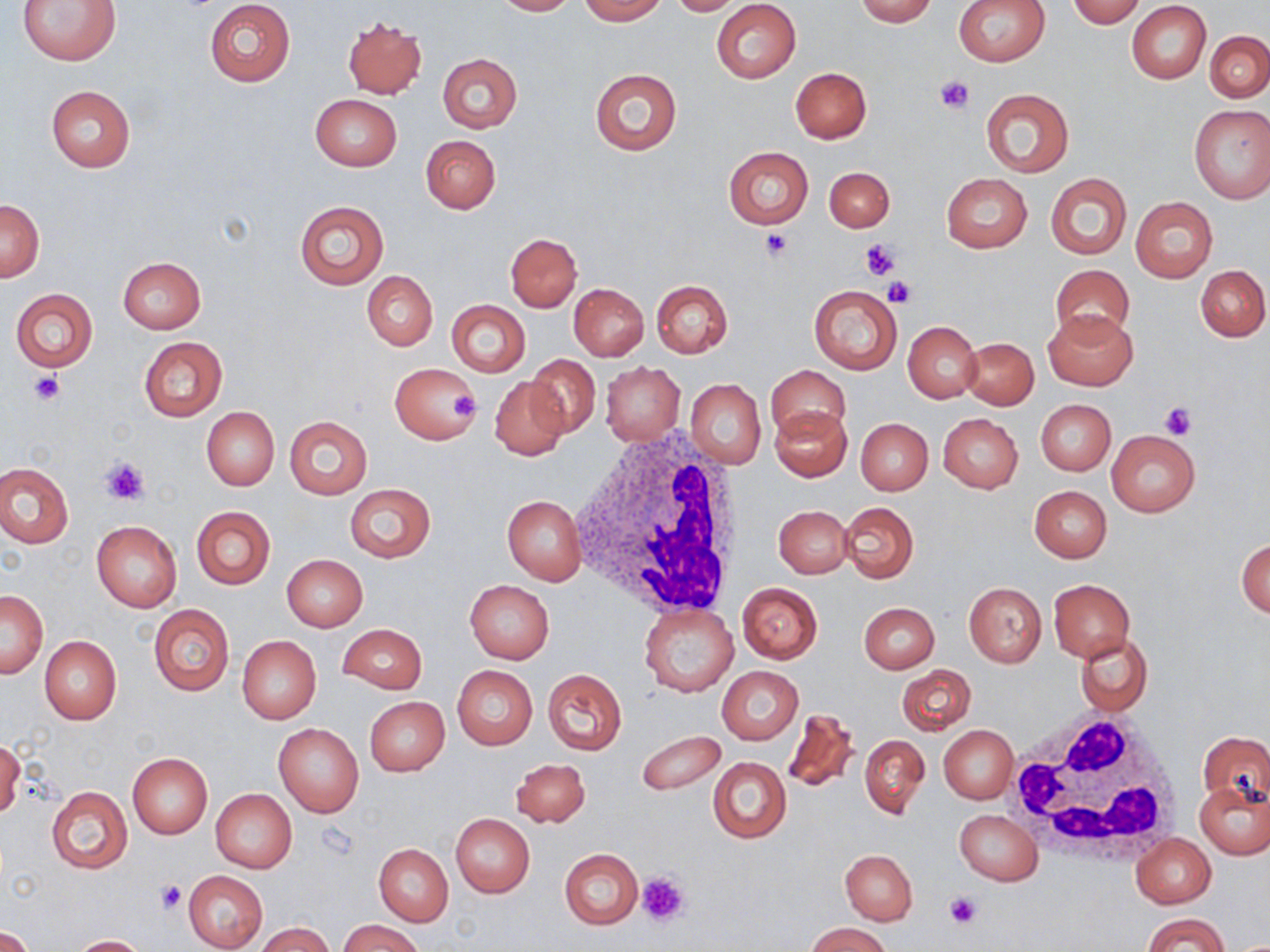
Summary:
  - Coordinate format: approximate bounding boxes as named x1/y1/x2/y2 corners in pixels
  - White blood cell locations: (x1=571, y1=430, x2=752, y2=614), (x1=1006, y1=706, x2=1189, y2=864)
  - Platelet locations: (x1=936, y1=74, x2=973, y2=113), (x1=760, y1=229, x2=793, y2=259), (x1=860, y1=238, x2=902, y2=279), (x1=885, y1=278, x2=916, y2=308), (x1=27, y1=371, x2=64, y2=406), (x1=451, y1=390, x2=477, y2=421), (x1=1160, y1=403, x2=1196, y2=440), (x1=99, y1=457, x2=151, y2=505), (x1=636, y1=870, x2=690, y2=927), (x1=156, y1=879, x2=185, y2=914), (x1=945, y1=890, x2=982, y2=928)
  - Uninfected red blood cell locations: (x1=17, y1=0, x2=123, y2=66), (x1=206, y1=0, x2=295, y2=87), (x1=494, y1=0, x2=576, y2=15), (x1=579, y1=0, x2=665, y2=23), (x1=667, y1=0, x2=746, y2=14), (x1=854, y1=0, x2=937, y2=25), (x1=954, y1=0, x2=1050, y2=66), (x1=1067, y1=0, x2=1146, y2=27), (x1=712, y1=1, x2=801, y2=83), (x1=1127, y1=3, x2=1211, y2=84), (x1=342, y1=16, x2=427, y2=99), (x1=1205, y1=32, x2=1270, y2=102), (x1=437, y1=53, x2=522, y2=132), (x1=790, y1=67, x2=871, y2=143), (x1=590, y1=68, x2=681, y2=155), (x1=46, y1=86, x2=136, y2=173), (x1=980, y1=88, x2=1074, y2=177), (x1=309, y1=94, x2=401, y2=170), (x1=1189, y1=105, x2=1270, y2=203), (x1=420, y1=134, x2=501, y2=213), (x1=723, y1=146, x2=813, y2=228), (x1=823, y1=166, x2=894, y2=233), (x1=1045, y1=172, x2=1132, y2=260), (x1=941, y1=173, x2=1032, y2=253), (x1=1131, y1=197, x2=1217, y2=282), (x1=294, y1=199, x2=390, y2=290), (x1=0, y1=200, x2=44, y2=282), (x1=506, y1=233, x2=581, y2=311), (x1=117, y1=257, x2=206, y2=334), (x1=1051, y1=264, x2=1135, y2=342), (x1=1196, y1=266, x2=1269, y2=341), (x1=370, y1=269, x2=448, y2=419), (x1=363, y1=271, x2=438, y2=350), (x1=651, y1=281, x2=734, y2=358), (x1=569, y1=282, x2=648, y2=361), (x1=809, y1=285, x2=901, y2=374), (x1=11, y1=288, x2=98, y2=371), (x1=446, y1=300, x2=530, y2=377), (x1=1044, y1=308, x2=1137, y2=390), (x1=903, y1=321, x2=982, y2=403), (x1=139, y1=336, x2=228, y2=421), (x1=962, y1=338, x2=1038, y2=409), (x1=526, y1=353, x2=600, y2=438), (x1=600, y1=361, x2=685, y2=445), (x1=389, y1=362, x2=481, y2=444), (x1=767, y1=365, x2=849, y2=440), (x1=489, y1=376, x2=569, y2=460), (x1=686, y1=379, x2=765, y2=469), (x1=1035, y1=399, x2=1115, y2=475), (x1=771, y1=404, x2=851, y2=481), (x1=201, y1=407, x2=279, y2=490), (x1=938, y1=413, x2=1023, y2=493), (x1=284, y1=415, x2=373, y2=499), (x1=855, y1=417, x2=932, y2=495), (x1=1106, y1=430, x2=1199, y2=515), (x1=0, y1=463, x2=73, y2=548), (x1=344, y1=484, x2=436, y2=563), (x1=1029, y1=485, x2=1111, y2=563), (x1=502, y1=495, x2=587, y2=585), (x1=840, y1=502, x2=918, y2=582), (x1=191, y1=505, x2=276, y2=589), (x1=773, y1=505, x2=852, y2=577), (x1=91, y1=521, x2=181, y2=612), (x1=1237, y1=538, x2=1270, y2=619), (x1=282, y1=554, x2=367, y2=632), (x1=1049, y1=579, x2=1134, y2=661), (x1=465, y1=580, x2=554, y2=663), (x1=963, y1=582, x2=1046, y2=667), (x1=737, y1=583, x2=822, y2=663), (x1=0, y1=589, x2=48, y2=678), (x1=859, y1=602, x2=939, y2=673), (x1=639, y1=603, x2=739, y2=696), (x1=149, y1=604, x2=233, y2=695), (x1=337, y1=623, x2=427, y2=694), (x1=1074, y1=633, x2=1153, y2=716), (x1=40, y1=636, x2=121, y2=724), (x1=238, y1=636, x2=321, y2=724), (x1=897, y1=663, x2=976, y2=734), (x1=452, y1=665, x2=537, y2=749), (x1=716, y1=666, x2=803, y2=744), (x1=543, y1=668, x2=627, y2=755), (x1=366, y1=696, x2=450, y2=776), (x1=783, y1=708, x2=859, y2=792), (x1=274, y1=723, x2=364, y2=817), (x1=940, y1=726, x2=1018, y2=803), (x1=636, y1=729, x2=726, y2=795), (x1=1199, y1=731, x2=1270, y2=808), (x1=859, y1=735, x2=929, y2=819), (x1=0, y1=740, x2=24, y2=819), (x1=128, y1=753, x2=212, y2=838), (x1=709, y1=756, x2=791, y2=843), (x1=512, y1=758, x2=590, y2=827), (x1=1196, y1=781, x2=1270, y2=859), (x1=47, y1=786, x2=132, y2=874), (x1=211, y1=788, x2=296, y2=873), (x1=954, y1=810, x2=1042, y2=885), (x1=450, y1=814, x2=535, y2=897), (x1=1132, y1=834, x2=1216, y2=908), (x1=373, y1=843, x2=453, y2=926), (x1=559, y1=848, x2=643, y2=930), (x1=840, y1=850, x2=917, y2=925), (x1=183, y1=870, x2=268, y2=952), (x1=1142, y1=913, x2=1228, y2=952), (x1=338, y1=920, x2=425, y2=952), (x1=804, y1=922, x2=894, y2=952), (x1=257, y1=923, x2=336, y2=952), (x1=1, y1=926, x2=34, y2=952), (x1=71, y1=935, x2=148, y2=952)
  - Slide-level diagnosis: no evidence of blood parasites
  - Modality: optical microscopy
  - Stain: May-Grünwald-Giemsa
  - Preparation: thin blood smear
  - Magnification: 1000x
  - Field of view: one of a larger specimen
  - Image size: 1270×952 pixels